Assess for parasitized red blood cells.
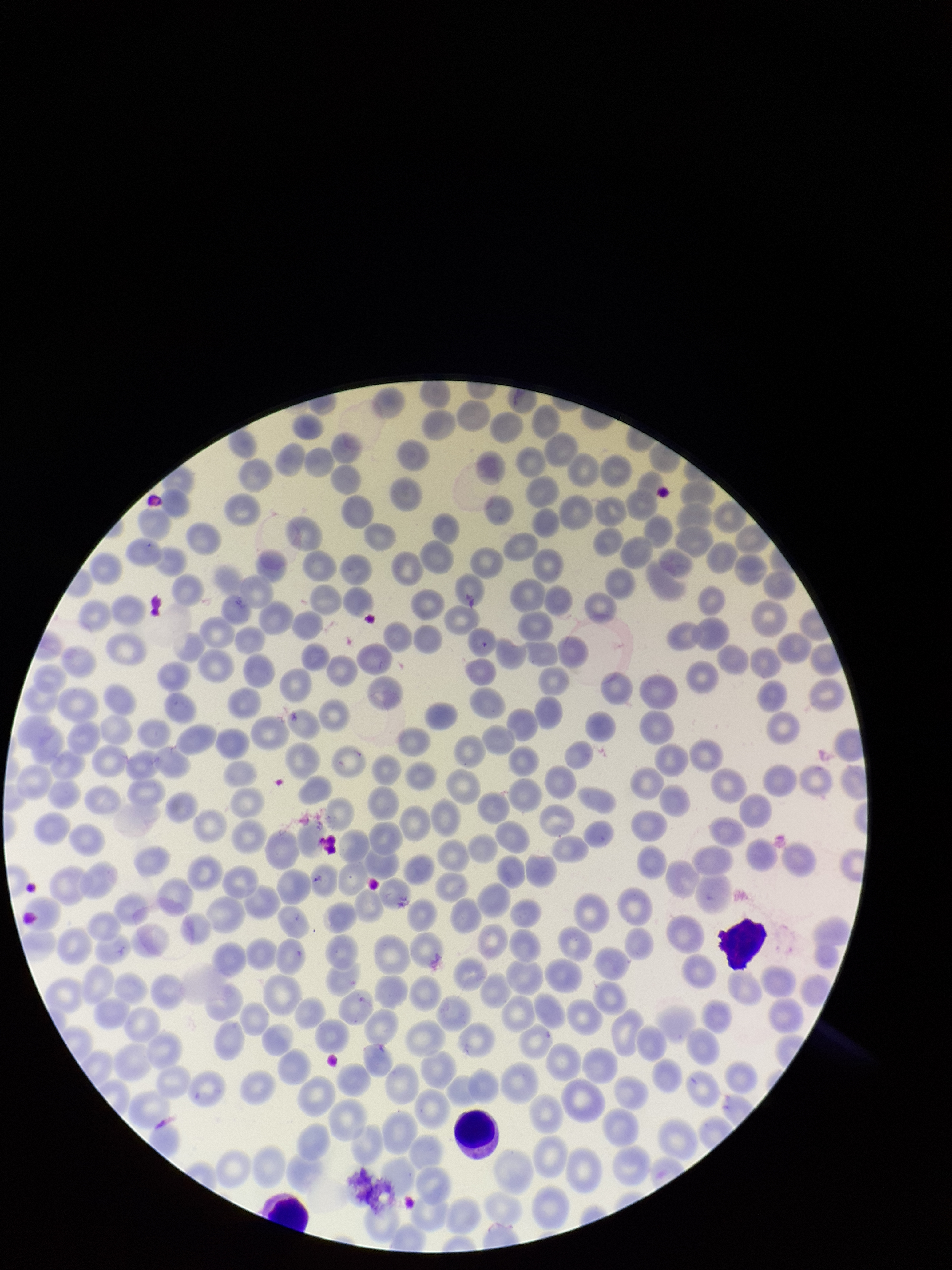
None detected.

species reported for this patient = Plasmodium vivax
parasitized red blood cell count = 0
stain = Giemsa
red blood cell count = 282
field of view = one from this slide
image size = 952×1270 pixels
capture = smartphone photograph through the microscope eyepiece
preparation = thin blood smear
patient malaria status = positive